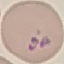
Malaria status: parasitized. Thin smear of blood. Photographed with a smartphone camera at the microscope eyepiece. Automatically extracted cell patch, resized to 64 × 64 pixels. Giemsa-stained preparation.